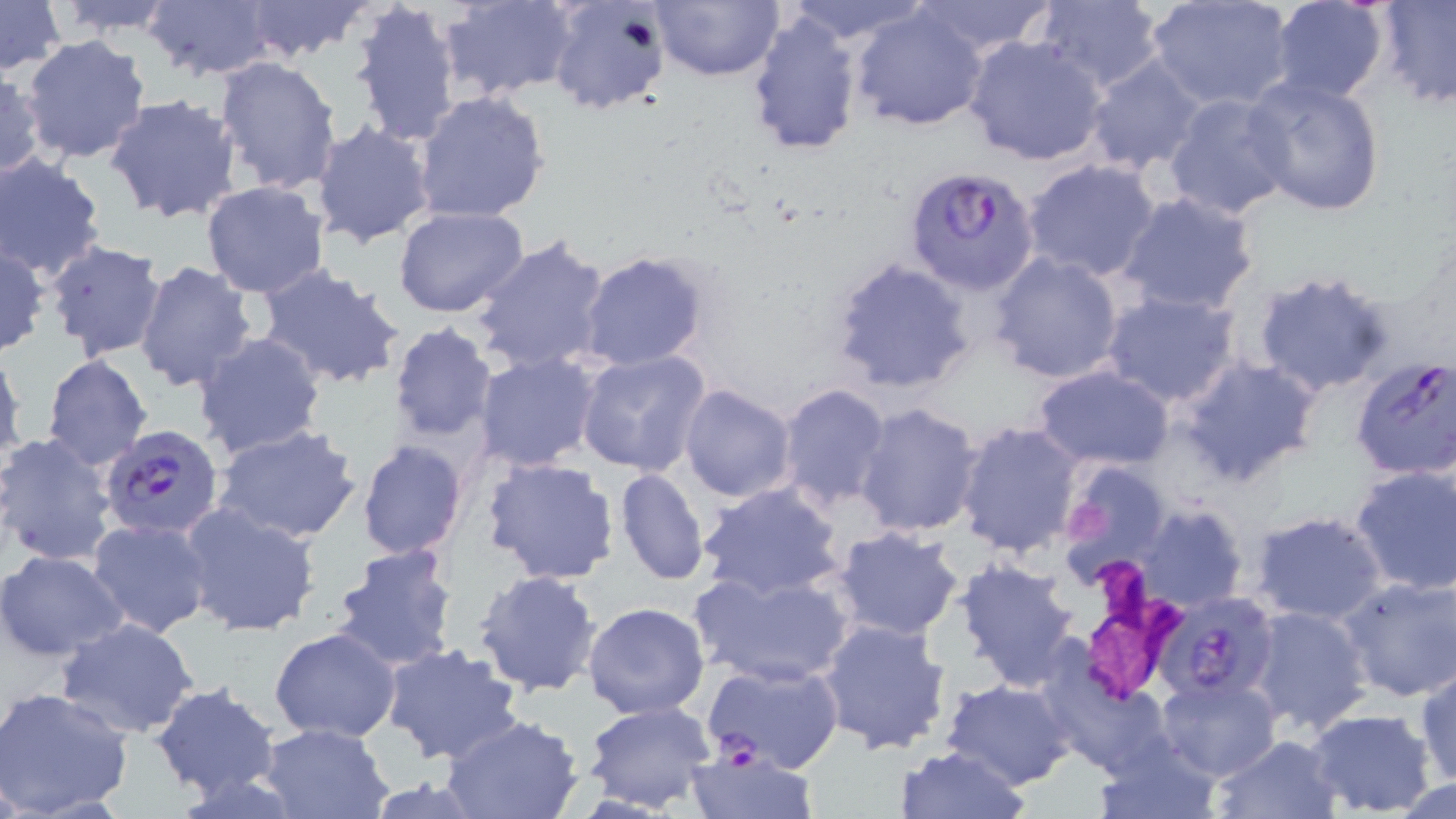 Approximate bounding boxes as [x1, y1, x2, y2] in pixels. Plasmodium falciparum-infected red blood cell locations: [905, 165, 1041, 294], [1350, 356, 1456, 480], [99, 423, 225, 540], [1156, 593, 1279, 703], [701, 657, 847, 773]. Platelet locations: [1067, 496, 1110, 550]. Uninfected red blood cell locations: [0, 0, 63, 77], [49, 0, 182, 36], [239, 0, 371, 63], [350, 0, 465, 149], [437, 0, 578, 104], [650, 0, 783, 83], [781, 0, 931, 44], [909, 0, 1059, 56], [1030, 0, 1166, 94], [1375, 0, 1456, 107], [142, 1, 278, 80], [1269, 1, 1390, 103], [546, 2, 669, 117], [1146, 2, 1293, 111], [850, 4, 990, 131], [745, 11, 865, 157], [19, 34, 152, 164], [963, 35, 1110, 166], [214, 55, 343, 195], [1084, 55, 1208, 175], [1, 72, 46, 181], [1243, 73, 1388, 219], [412, 90, 552, 226], [1162, 91, 1296, 223], [102, 94, 243, 226], [311, 121, 435, 248], [0, 155, 109, 281], [1021, 158, 1165, 283], [201, 180, 331, 299], [1115, 191, 1262, 316], [393, 206, 527, 316], [470, 235, 612, 377], [42, 238, 167, 361], [0, 241, 49, 357], [577, 250, 708, 370], [986, 250, 1126, 385], [824, 255, 976, 396], [133, 260, 257, 396], [254, 262, 406, 391], [1252, 270, 1397, 401], [1099, 289, 1245, 411], [387, 321, 498, 448], [192, 331, 328, 461], [0, 344, 25, 473], [574, 350, 713, 478], [474, 352, 602, 472], [42, 354, 152, 471], [1176, 355, 1323, 487], [1033, 365, 1175, 471], [678, 383, 797, 502], [774, 383, 891, 513], [853, 401, 986, 538], [954, 420, 1083, 558], [211, 424, 363, 545], [0, 433, 117, 565], [357, 439, 470, 561], [480, 456, 621, 586], [1061, 461, 1178, 575], [1351, 464, 1456, 597], [614, 467, 709, 585], [697, 482, 847, 600], [178, 502, 320, 639], [1137, 502, 1248, 612], [1248, 510, 1389, 626], [86, 516, 213, 638], [833, 526, 965, 641], [330, 543, 460, 674], [0, 549, 129, 661], [952, 558, 1083, 692], [688, 564, 858, 689], [475, 569, 601, 698], [1338, 576, 1455, 703], [582, 600, 710, 719], [1244, 605, 1373, 735], [814, 616, 954, 757], [55, 617, 201, 739], [269, 627, 401, 743], [380, 643, 523, 764], [1416, 665, 1456, 789], [1157, 672, 1280, 781], [940, 677, 1077, 789], [1063, 680, 1189, 803], [151, 683, 281, 802], [0, 686, 134, 817], [582, 700, 718, 813], [1304, 708, 1437, 816], [438, 713, 587, 819], [254, 722, 395, 819], [1209, 733, 1343, 819], [1095, 735, 1223, 819], [684, 745, 817, 818], [895, 745, 1028, 819], [1388, 774, 1456, 818]. Slide-level diagnosis: Plasmodium falciparum. May-Grünwald-Giemsa-stained preparation. One field of a larger specimen. Thin blood film. 1000x magnification. Image is 1456×819 pixels. Light microscopy.